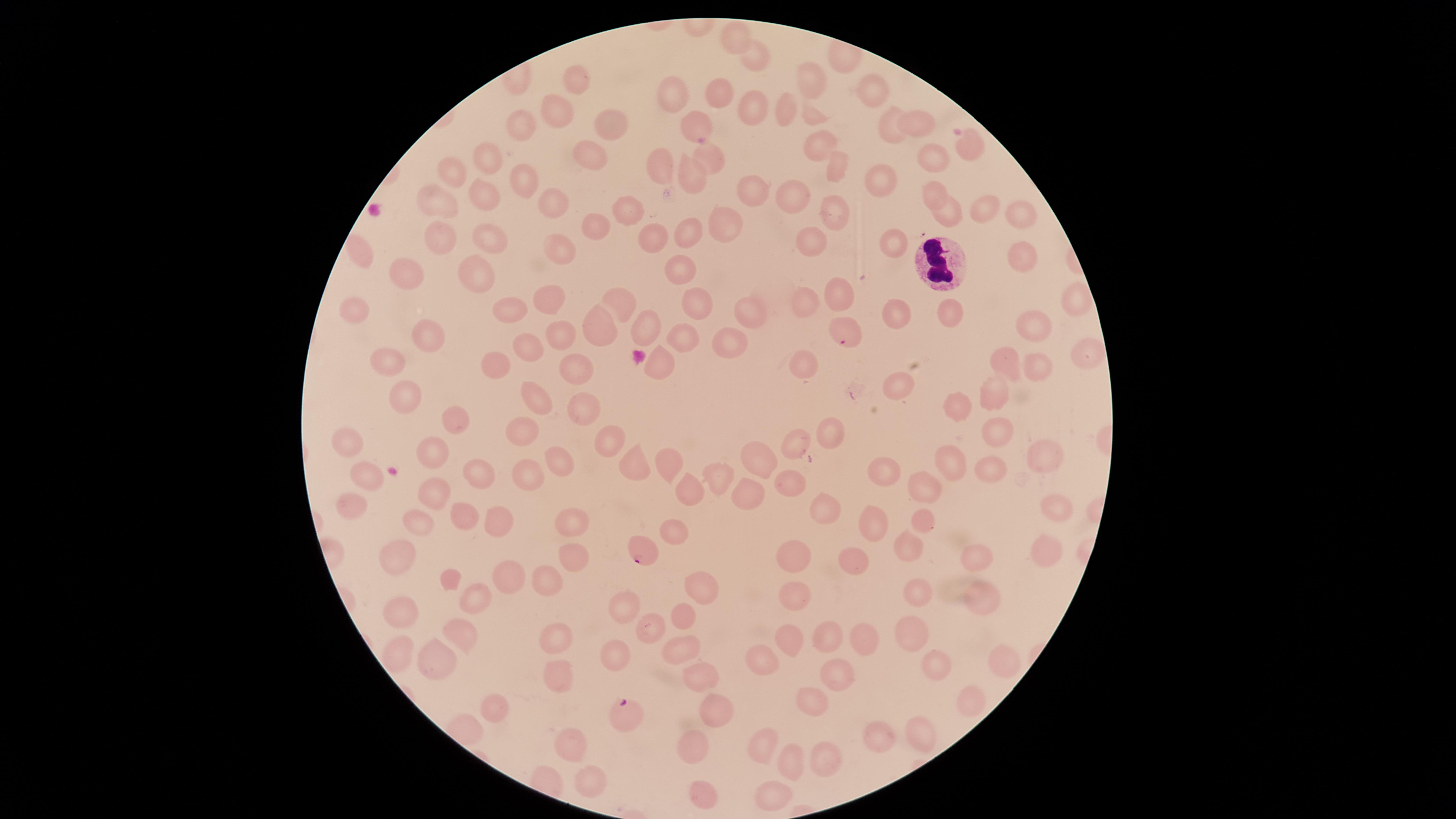

field_of_view: single
white_blood_cells: 'approximate marker points as [x, y] in pixels: [943, 262]'
species: Plasmodium falciparum
parasitized_red_blood_cells: 'approximate marker points as [x, y] in pixels: [844, 332], [641, 550], [623, 713]'
capture: smartphone photograph through the microscope eyepiece
uninfected_red_blood_cells: 'approximate marker points as [x, y] in pixels: [734, 37], [757, 58], [574, 79], [810, 79], [873, 91], [873, 92], [671, 93], [714, 96], [753, 107], [555, 108], [785, 108], [809, 118], [919, 122], [892, 124], [692, 125], [521, 127], [604, 127], [969, 140], [817, 145], [591, 152], [490, 154], [709, 157], [932, 161], [660, 169], [835, 169], [455, 179], [692, 180], [524, 182], [881, 185], [488, 195], [932, 195], [750, 196], [791, 201], [552, 202], [442, 203], [622, 211], [982, 211], [947, 213], [1024, 213], [835, 214], [598, 223], [687, 226], [723, 228], [489, 237], [439, 240], [656, 240], [817, 240], [557, 246], [895, 247], [1023, 258], [678, 267], [478, 271], [407, 273], [836, 292], [551, 298], [620, 305], [691, 305], [1077, 306], [802, 307], [755, 309], [359, 310], [503, 312], [951, 312], [898, 317], [650, 322], [1033, 325], [599, 327], [426, 336], [681, 339], [562, 340], [732, 342], [527, 347], [1089, 354], [391, 356], [496, 359], [1008, 361], [654, 362], [569, 363], [804, 370], [1036, 372], [896, 384], [995, 393], [406, 396], [956, 403], [537, 406], [581, 407], [452, 420], [516, 432], [832, 433], [997, 434], [611, 439], [347, 441], [797, 442], [436, 449], [949, 456], [758, 458], [1043, 459], [561, 461], [670, 464], [631, 465], [481, 471], [369, 472], [995, 473], [526, 474], [886, 474], [714, 479], [786, 483], [436, 490], [689, 490], [924, 490], [742, 493], [351, 501], [826, 507], [1054, 509], [461, 515], [419, 519], [924, 519], [494, 522], [875, 523], [569, 524], [673, 528], [910, 542], [1042, 548], [397, 552], [567, 558], [978, 558], [794, 559], [851, 562], [507, 575], [448, 578], [544, 581], [701, 587], [920, 591], [981, 595], [469, 596], [793, 596], [627, 602], [396, 611], [681, 613], [651, 626], [910, 634], [458, 637], [826, 637], [787, 638], [557, 639], [860, 641], [681, 651], [396, 652], [436, 654], [617, 654], [931, 660], [1002, 660], [757, 664], [554, 673], [699, 676], [832, 676], [973, 700], [813, 701], [496, 706], [714, 707], [920, 729], [880, 736], [694, 740], [572, 743], [760, 744], [822, 756], [790, 761], [591, 781], [699, 793], [772, 793]'
visible_region: circular
stain: Giemsa
presence: malaria parasites identified
image_size: 1456×819 pixels
preparation: thin blood smear